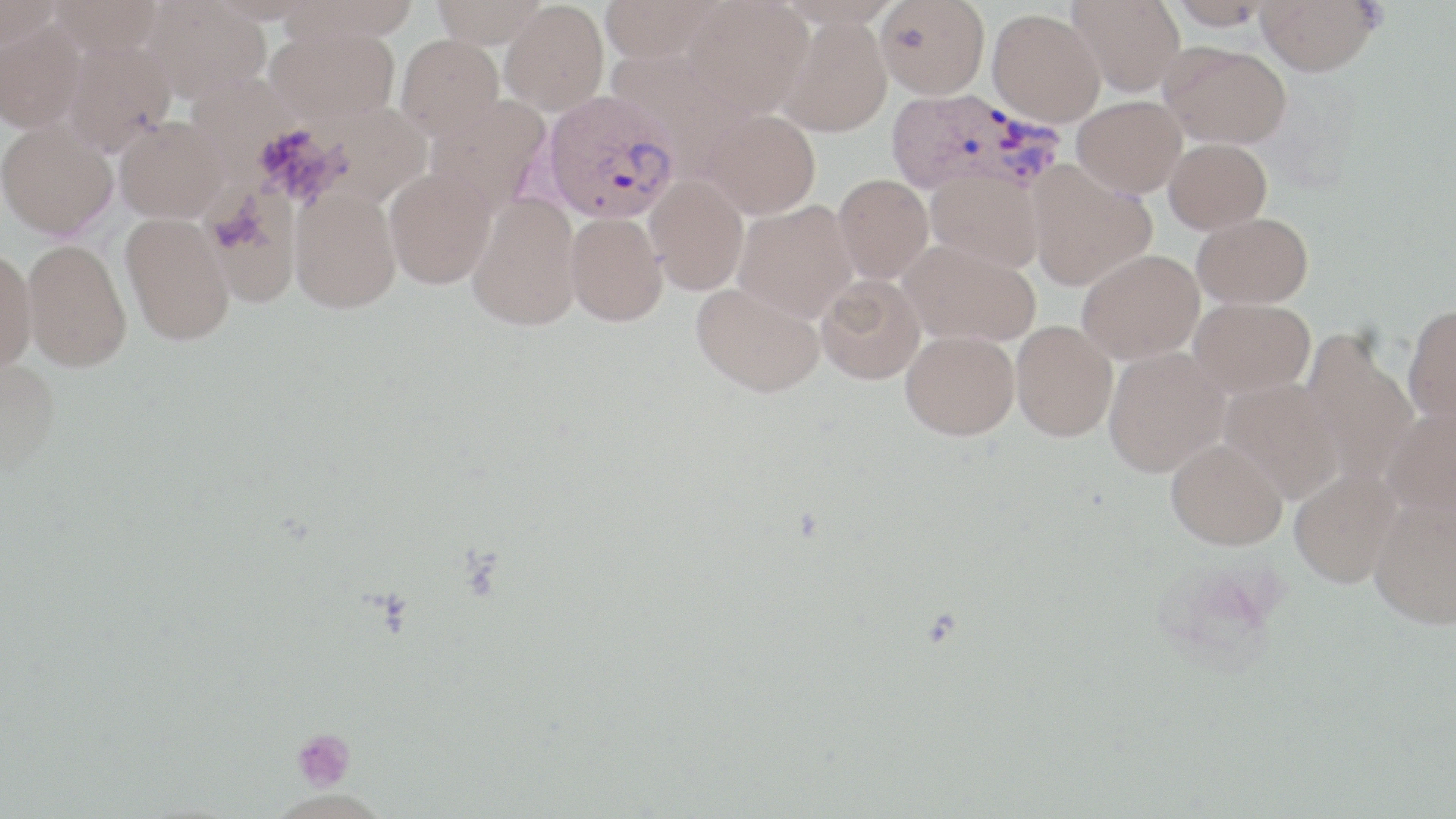
slide-level diagnosis = Plasmodium vivax
image size = 1456×819 pixels
uninfected red blood cell locations = approximate bounding boxes as (x1, y1, x2, y2) in pixels: (0, 0, 61, 53), (48, 0, 164, 58), (142, 0, 270, 102), (281, 0, 420, 43), (430, 0, 550, 48), (599, 0, 727, 64), (684, 0, 813, 117), (875, 0, 990, 99), (1067, 0, 1186, 97), (1168, 0, 1275, 29), (1256, 0, 1381, 75), (500, 1, 609, 116), (775, 1, 903, 28), (988, 9, 1106, 127), (776, 15, 893, 137), (0, 17, 86, 133), (266, 24, 400, 128), (396, 34, 504, 139), (62, 40, 176, 155), (1159, 40, 1292, 147), (425, 95, 552, 217), (1072, 96, 1186, 198), (703, 108, 821, 219), (116, 117, 228, 222), (0, 119, 117, 238), (1165, 138, 1271, 233), (1027, 162, 1157, 291), (384, 167, 497, 289), (925, 169, 1044, 271), (833, 174, 933, 284), (645, 175, 749, 295), (204, 178, 307, 308), (289, 189, 401, 313), (467, 192, 582, 330), (733, 201, 857, 322), (120, 212, 236, 345), (565, 212, 668, 326), (1192, 212, 1313, 308), (22, 238, 131, 371), (900, 240, 1040, 347), (0, 248, 37, 373), (1077, 249, 1204, 364), (816, 274, 925, 384), (691, 281, 825, 397), (1189, 297, 1314, 398), (1403, 304, 1456, 424), (1011, 320, 1117, 441), (1301, 327, 1419, 486), (901, 330, 1019, 440), (1102, 346, 1231, 477), (0, 356, 60, 474), (1219, 378, 1344, 502), (1381, 408, 1456, 517), (1166, 437, 1288, 550), (1289, 467, 1402, 587), (1368, 497, 1456, 629)
field of view = single
stain = May-Grünwald-Giemsa
modality = light microscopy
preparation = thin blood film
magnification = 1000x
platelet locations = approximate bounding boxes as (x1, y1, x2, y2) in pixels: (291, 728, 356, 793)
Plasmodium vivax-infected red blood cell locations = approximate bounding boxes as (x1, y1, x2, y2) in pixels: (884, 87, 1064, 198), (542, 92, 681, 225)